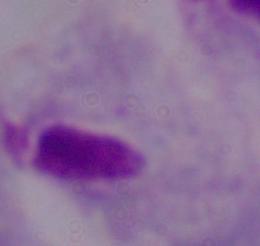
1000x magnification. Micrograph. A trichomonad is seen.